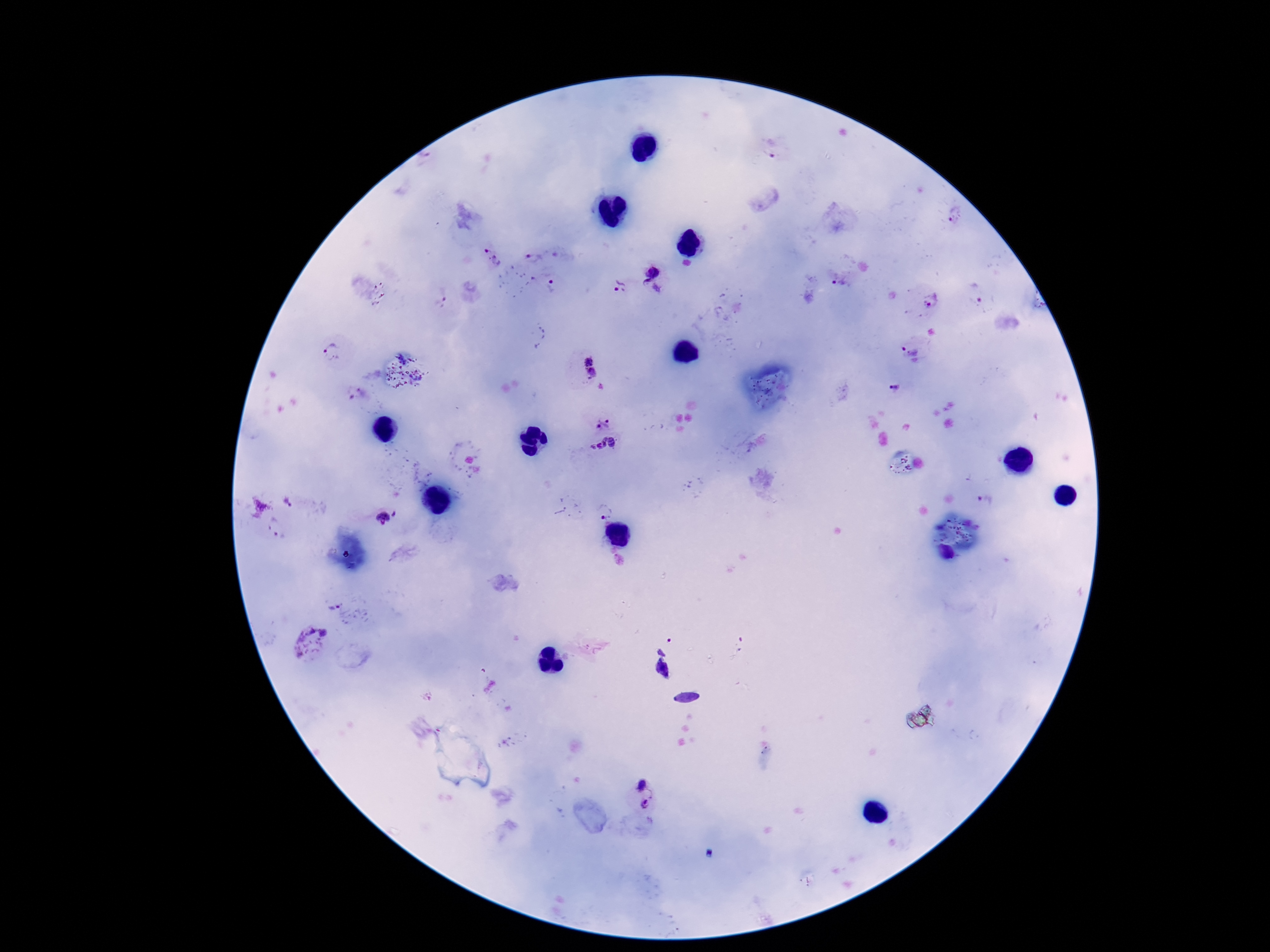

Approximate centers as [x, y] in pixels. Plasmodium parasite locations: [769, 153], [951, 219], [486, 251], [529, 256], [653, 270], [550, 281], [619, 285], [838, 285], [652, 289], [978, 293], [933, 300], [903, 349], [333, 351], [588, 360], [592, 373], [894, 387], [603, 423], [605, 447], [986, 500], [289, 503], [604, 510], [396, 513], [383, 518], [276, 527], [334, 606], [308, 639], [643, 785], [645, 803]. Image is 1270×952 pixels. Thick peripheral-blood smear. Patient malaria status: infected. Smartphone photograph taken through the microscope eyepiece. Giemsa stain. One field from this slide. 100x magnification.